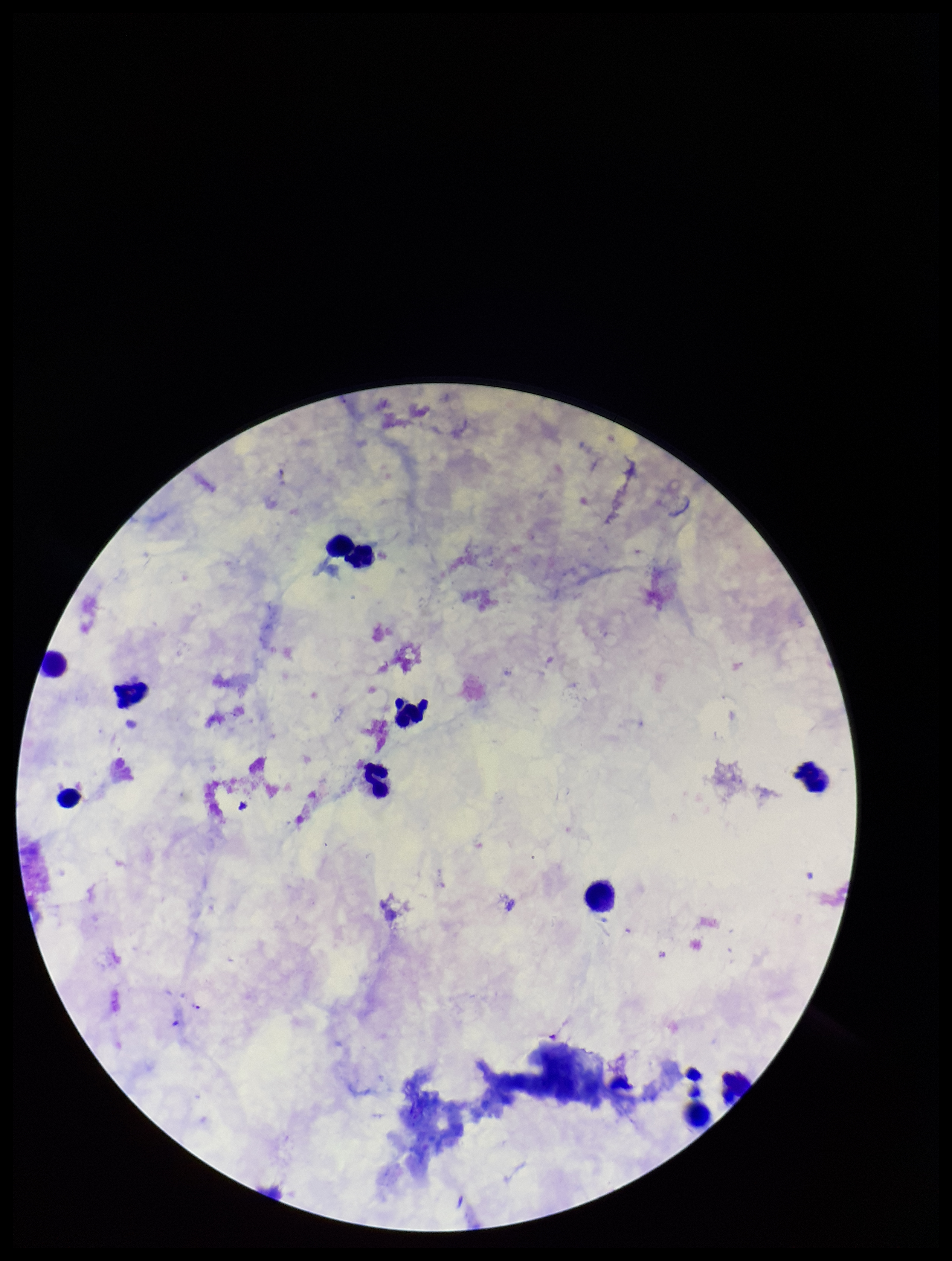
Summary:
  - Patient malaria status: infected
  - Capture: smartphone photograph through the microscope eyepiece
  - Field of view: single
  - Plasmodium parasites: detected
  - Preparation: thick
  - Species reported for this patient: Plasmodium falciparum
  - Stain: Giemsa
  - Leukocyte count: 12
  - Image size: 952×1261 pixels
  - Parasite count: 1